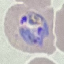

Summary:
  - Malaria status: parasitized
  - Stain: Giemsa
  - Image type: cell patch, automatically extracted from a larger field of view and resized to 64 × 64 pixels
  - Capture: smartphone through the microscope eyepiece
  - Preparation: thin blood film